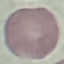
result = no malaria parasites seen
image type = cell patch, automatically extracted from a larger field of view and resized to 64 × 64 pixels
stain = Giemsa
capture = smartphone camera at the microscope eyepiece
preparation = thin smear